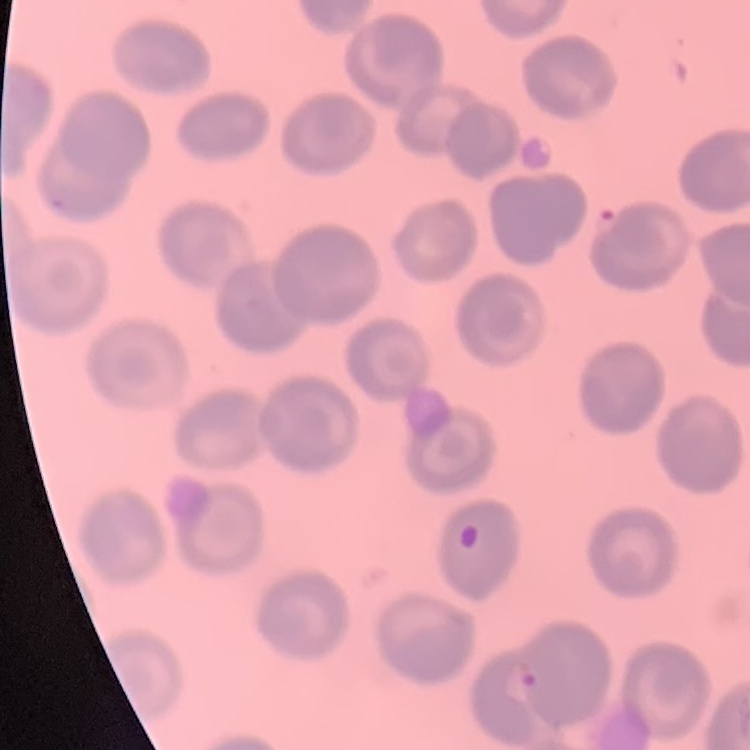
The red blood cells show no rouleaux formation. Stained with either Field's or Giemsa. One tile cut from a larger photomicrograph. Thin peripheral smear.